State which cell type is depicted.
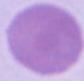
An erythrocyte.

Summary:
  - Magnification: 1000x
  - Modality: micrograph